Assess this cell for malaria.
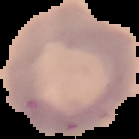

It is uninfected.

Summary:
  - Preparation: thin blood film
  - Image size: 139×139 pixels
  - Image type: segmented cell region on a black background